Identify the parasite.
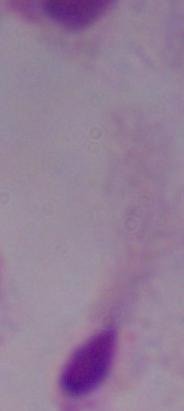

A trichomonad.

Micrograph. Captured at 1000x magnification.